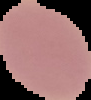

Summary:
  - Preparation: thin blood film
  - Image type: segmented cell region with the area outside set to black
  - Result: no malaria parasites seen
  - Image size: 91×100 pixels